Give the position of every malaria parasite.
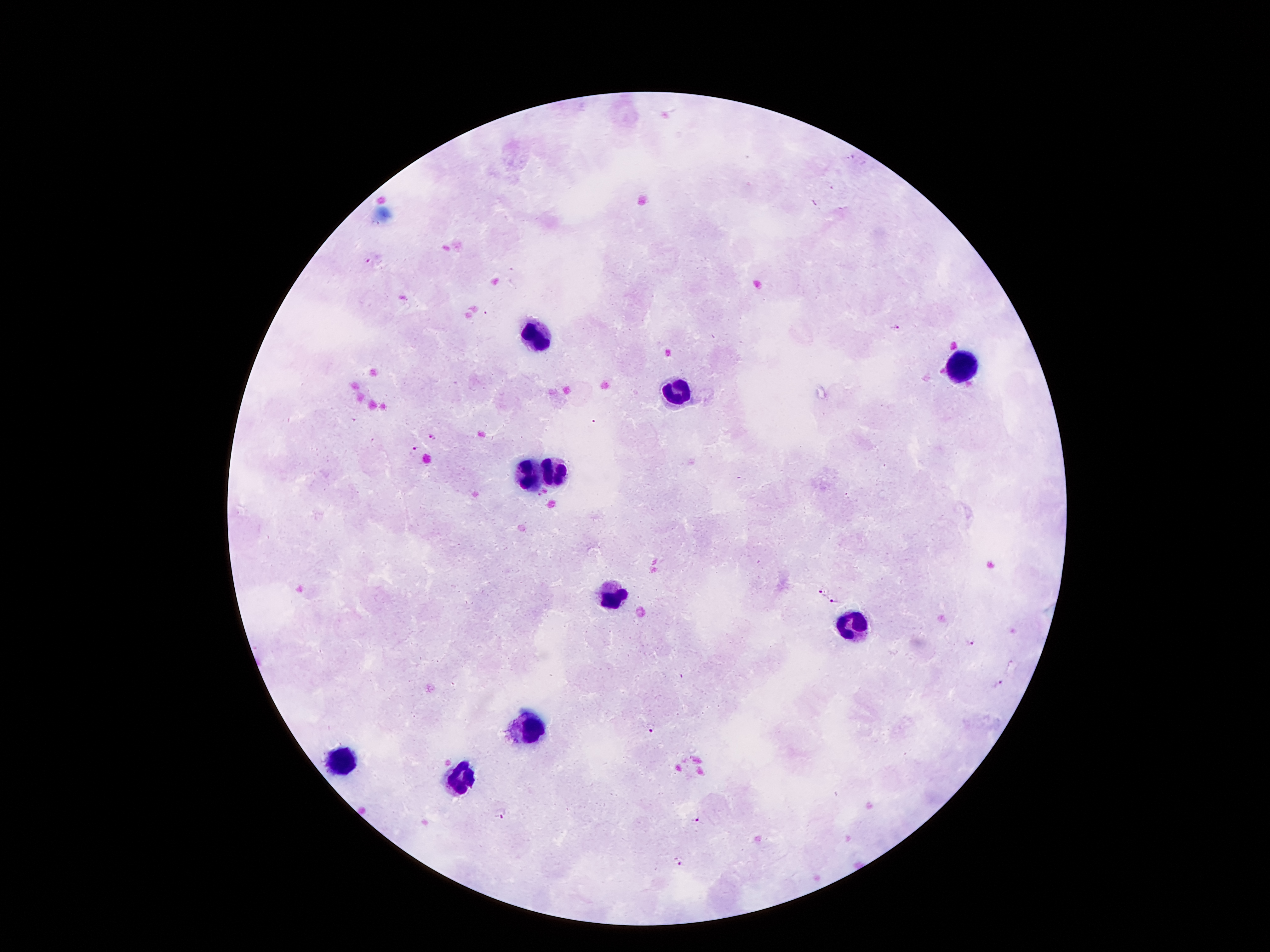
Approximate centers as {x, y} in pixels.
Malaria parasites: {366, 260}, {895, 328}, {435, 437}, {415, 449}, {821, 594}, {834, 602}, {970, 642}, {999, 684}, {652, 729}, {499, 813}, {698, 822}, {677, 862}.

leukocyte locations = {532, 335}, {960, 370}, {679, 393}, {552, 469}, {528, 477}, {614, 596}, {851, 626}, {528, 725}, {345, 759}, {460, 780}
magnification = 100x
field of view = one from this slide
patient malaria status = positive for Plasmodium falciparum
image size = 1270×952 pixels
capture = smartphone through the microscope eyepiece
preparation = thick blood film
stain = Giemsa